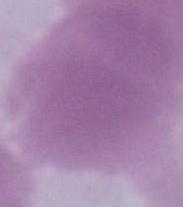
modality = photomicrograph
identification = red blood cell
magnification = 1000x